Assess this cell for malaria.
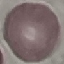

It is uninfected.

Summary:
  - Image type: cell patch, automatically extracted from a larger field of view and resized to 64 × 64 pixels
  - Stain: Giemsa
  - Capture: smartphone through the microscope eyepiece
  - Preparation: thin blood smear